Locate and identify every blood parasite.
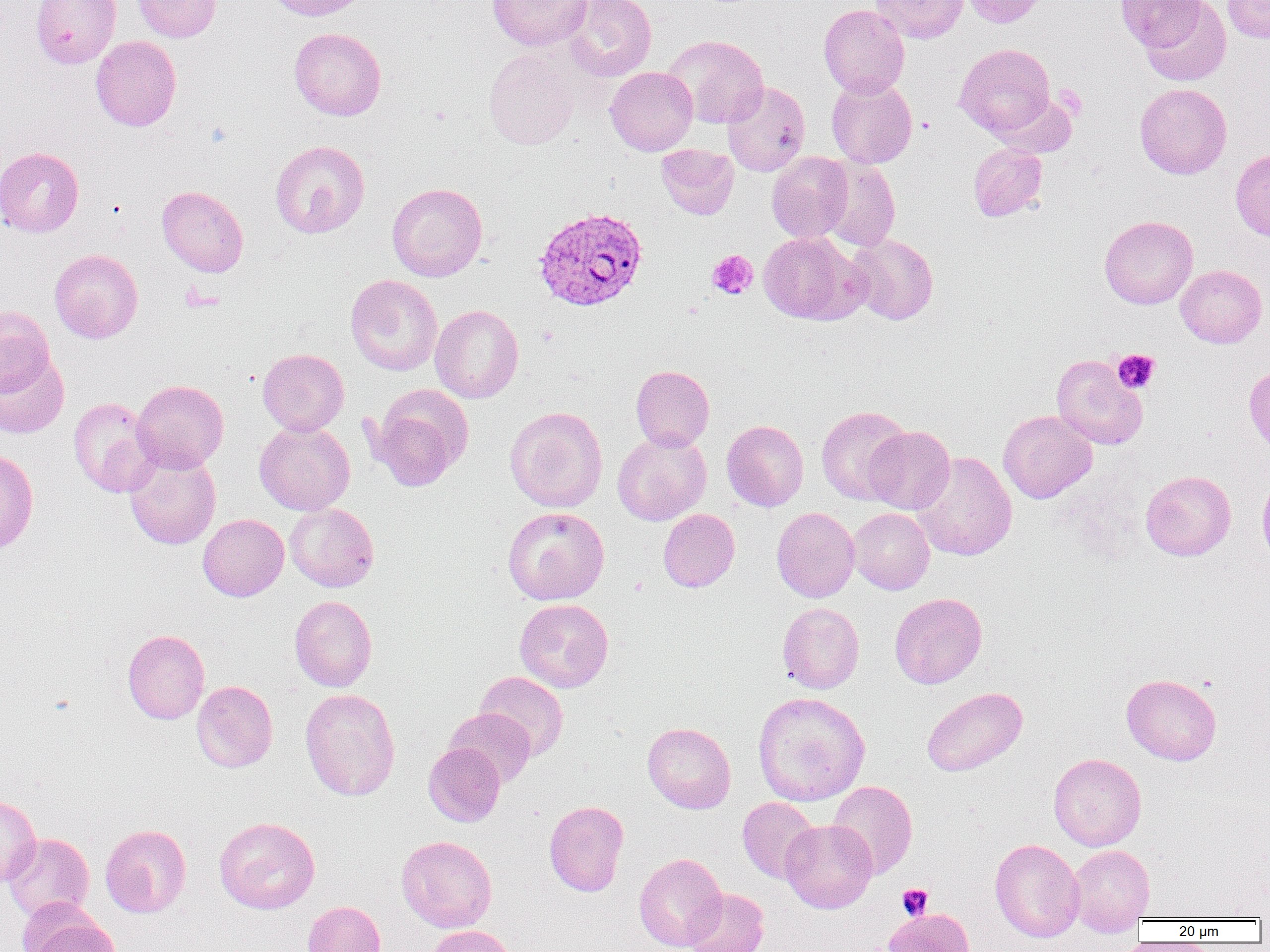
Approximate bounding boxes as named x1/y1/x2/y2 corners in pixels.
Plasmodium vivax-infected red blood cells: (x1=532, y1=205, x2=648, y2=312).
No Plasmodium falciparum, Plasmodium ovale, Plasmodium malariae, Babesia divergens, or Trypanosoma brucei observed.

slide-level diagnosis = Plasmodium vivax
modality = optical microscopy
uninfected red blood cell locations = approximate bounding boxes as named x1/y1/x2/y2 corners in pixels: (x1=30, y1=0, x2=121, y2=68), (x1=132, y1=0, x2=221, y2=42), (x1=264, y1=0, x2=370, y2=21), (x1=488, y1=0, x2=592, y2=51), (x1=564, y1=0, x2=656, y2=81), (x1=870, y1=0, x2=968, y2=43), (x1=962, y1=0, x2=1048, y2=28), (x1=1116, y1=0, x2=1203, y2=52), (x1=1222, y1=0, x2=1270, y2=43), (x1=1140, y1=1, x2=1231, y2=86), (x1=819, y1=4, x2=909, y2=98), (x1=289, y1=27, x2=387, y2=120), (x1=663, y1=35, x2=769, y2=129), (x1=91, y1=36, x2=181, y2=131), (x1=955, y1=43, x2=1056, y2=138), (x1=484, y1=48, x2=581, y2=149), (x1=604, y1=67, x2=697, y2=155), (x1=826, y1=76, x2=917, y2=168), (x1=722, y1=81, x2=810, y2=177), (x1=1134, y1=83, x2=1232, y2=179), (x1=270, y1=140, x2=370, y2=238), (x1=968, y1=143, x2=1047, y2=221), (x1=656, y1=144, x2=739, y2=220), (x1=0, y1=146, x2=84, y2=237), (x1=1230, y1=148, x2=1270, y2=242), (x1=766, y1=152, x2=853, y2=242), (x1=818, y1=158, x2=901, y2=251), (x1=387, y1=182, x2=487, y2=281), (x1=157, y1=185, x2=248, y2=276), (x1=1099, y1=216, x2=1198, y2=309), (x1=758, y1=231, x2=867, y2=325), (x1=847, y1=232, x2=938, y2=325), (x1=49, y1=249, x2=143, y2=343), (x1=1176, y1=265, x2=1267, y2=348), (x1=346, y1=274, x2=443, y2=376), (x1=430, y1=304, x2=523, y2=403), (x1=0, y1=305, x2=54, y2=396), (x1=257, y1=348, x2=349, y2=436), (x1=0, y1=354, x2=70, y2=439), (x1=1051, y1=354, x2=1147, y2=450), (x1=1244, y1=364, x2=1270, y2=457), (x1=630, y1=365, x2=715, y2=451), (x1=132, y1=379, x2=229, y2=472), (x1=370, y1=386, x2=472, y2=490), (x1=67, y1=397, x2=159, y2=498), (x1=505, y1=406, x2=608, y2=513), (x1=815, y1=406, x2=912, y2=504), (x1=998, y1=410, x2=1097, y2=503), (x1=722, y1=420, x2=808, y2=512), (x1=254, y1=421, x2=355, y2=515), (x1=864, y1=426, x2=955, y2=514), (x1=612, y1=431, x2=712, y2=525), (x1=0, y1=448, x2=39, y2=554), (x1=124, y1=448, x2=221, y2=549), (x1=912, y1=451, x2=1017, y2=561), (x1=1140, y1=470, x2=1236, y2=561), (x1=1257, y1=473, x2=1270, y2=567), (x1=284, y1=503, x2=379, y2=592), (x1=502, y1=507, x2=610, y2=605), (x1=772, y1=507, x2=859, y2=602), (x1=848, y1=508, x2=934, y2=594), (x1=658, y1=509, x2=739, y2=592), (x1=198, y1=514, x2=288, y2=601), (x1=889, y1=592, x2=987, y2=689), (x1=289, y1=595, x2=377, y2=691), (x1=514, y1=598, x2=613, y2=692), (x1=777, y1=602, x2=864, y2=693), (x1=122, y1=629, x2=209, y2=724), (x1=475, y1=671, x2=569, y2=761), (x1=1121, y1=673, x2=1221, y2=765), (x1=192, y1=680, x2=278, y2=772), (x1=922, y1=687, x2=1028, y2=776), (x1=300, y1=688, x2=400, y2=801), (x1=752, y1=691, x2=870, y2=806), (x1=445, y1=708, x2=536, y2=787), (x1=642, y1=722, x2=736, y2=813), (x1=423, y1=742, x2=505, y2=827), (x1=1048, y1=753, x2=1147, y2=851), (x1=827, y1=780, x2=918, y2=878), (x1=0, y1=794, x2=41, y2=887), (x1=737, y1=797, x2=819, y2=883), (x1=544, y1=801, x2=629, y2=896), (x1=214, y1=816, x2=320, y2=914), (x1=780, y1=819, x2=878, y2=913), (x1=100, y1=824, x2=191, y2=917), (x1=3, y1=833, x2=94, y2=922), (x1=396, y1=835, x2=497, y2=932), (x1=989, y1=838, x2=1085, y2=942), (x1=1068, y1=845, x2=1155, y2=934), (x1=633, y1=853, x2=727, y2=951), (x1=683, y1=888, x2=769, y2=952), (x1=302, y1=900, x2=386, y2=952), (x1=20, y1=906, x2=117, y2=952), (x1=883, y1=908, x2=974, y2=952), (x1=424, y1=925, x2=518, y2=952)
field of view = one of a larger specimen
preparation = thin blood film
magnification = 1000x
platelet locations = approximate bounding boxes as named x1/y1/x2/y2 corners in pixels: (x1=1053, y1=84, x2=1087, y2=119), (x1=706, y1=250, x2=758, y2=300), (x1=1112, y1=349, x2=1159, y2=393), (x1=897, y1=884, x2=933, y2=920)
image size = 1270×952 pixels